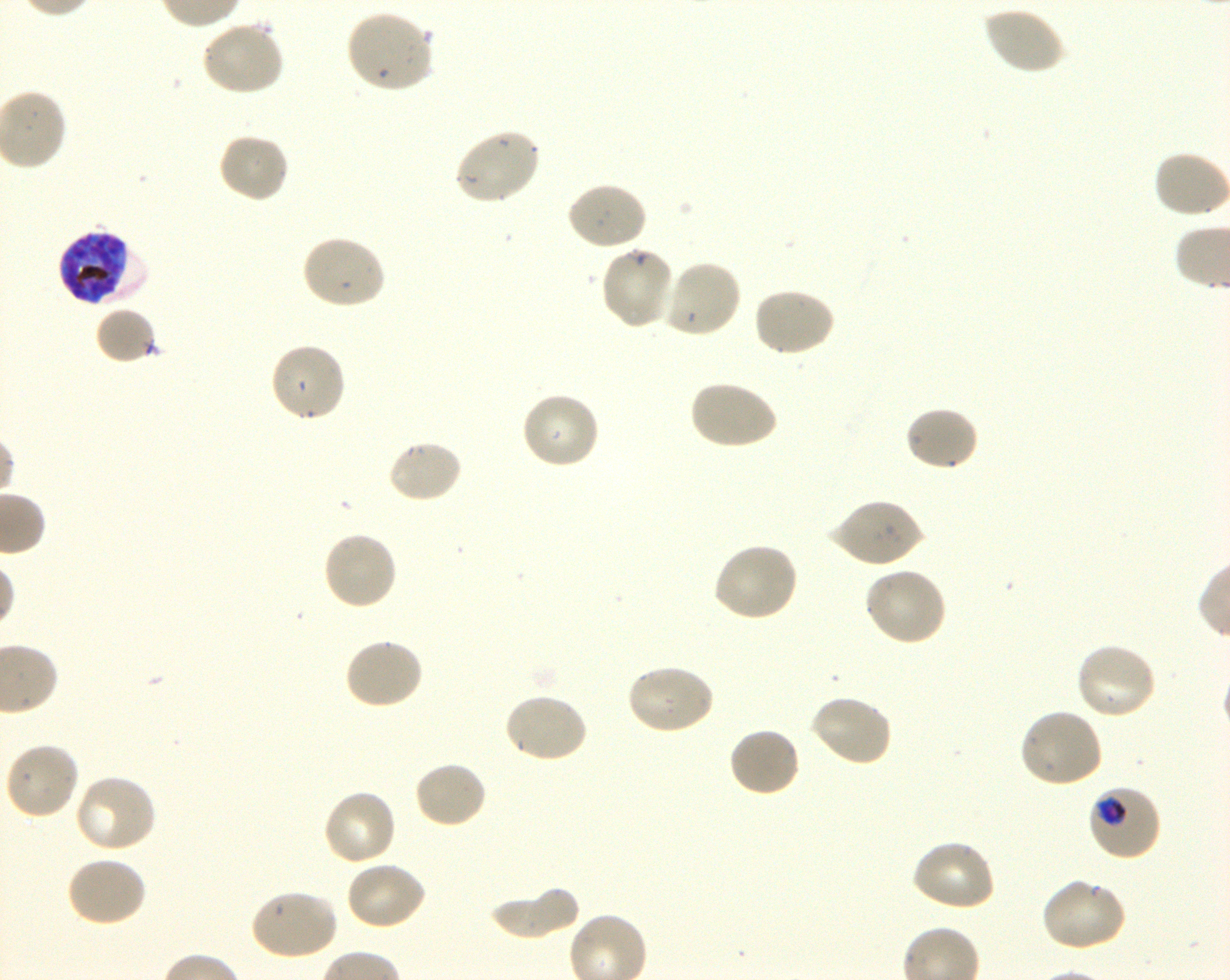

Not every red blood cell is marked. A life-cycle stage — or a range of stages, where the recorded stages span more than one — follows each staged infected red blood cell.
preparation: thin blood smear
image_size: 1230×980 pixels
stain: Giemsa
field_of_view: single
donor_blood_group: O+
locations_of_uninfected_red_blood_cells: 'approximate bounding boxes as [x1, y1, x2, y2] in pixels: [982, 5, 1066, 76], [344, 9, 435, 93], [201, 21, 286, 98], [453, 128, 542, 206], [216, 132, 290, 204], [1152, 150, 1230, 220], [564, 181, 649, 252], [301, 234, 387, 311], [598, 246, 676, 331], [660, 258, 741, 339], [752, 287, 836, 358], [95, 306, 159, 363], [269, 342, 348, 424], [688, 379, 778, 451], [520, 390, 601, 470], [906, 405, 979, 473], [387, 439, 464, 504], [829, 498, 924, 569], [321, 531, 398, 612], [712, 542, 800, 623], [863, 566, 948, 648], [344, 636, 425, 710], [1074, 642, 1158, 721], [625, 663, 715, 736], [502, 692, 589, 765], [808, 693, 893, 767], [1018, 708, 1105, 788], [727, 725, 802, 798], [4, 741, 80, 820], [413, 760, 488, 829], [73, 773, 158, 855], [322, 788, 397, 867], [911, 838, 997, 913], [64, 856, 147, 929], [344, 860, 427, 931], [1039, 877, 1127, 952], [488, 883, 580, 939], [249, 888, 339, 962]'
locations_of_infected_red_blood_cells: 'approximate bounding boxes as [x1, y1, x2, y2] in pixels: [57, 229, 146, 307] late trophozoite to late schizont; [1086, 783, 1161, 862] trophozoite'
objective: 100x, oil immersion, numerical aperture 1.30
culture: in-vitro P. falciparum strain 3D7, shaking